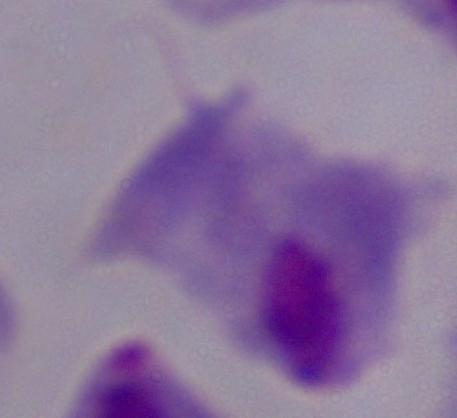

Summary:
  - Magnification: 1000x
  - Modality: photomicrograph
  - Identification: trichomonad